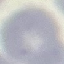
Malaria status: uninfected. Thin blood smear. Photographed with a smartphone camera at the microscope eyepiece. Giemsa-stained preparation. Automatically extracted cell patch, resized to 64 × 64 pixels.